Identify the parasite.
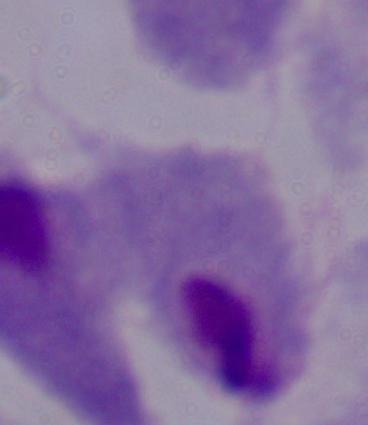
A trichomonad.

{
  "magnification": "1000x",
  "modality": "micrograph"
}